Give the extent of all uninfected red blood cells.
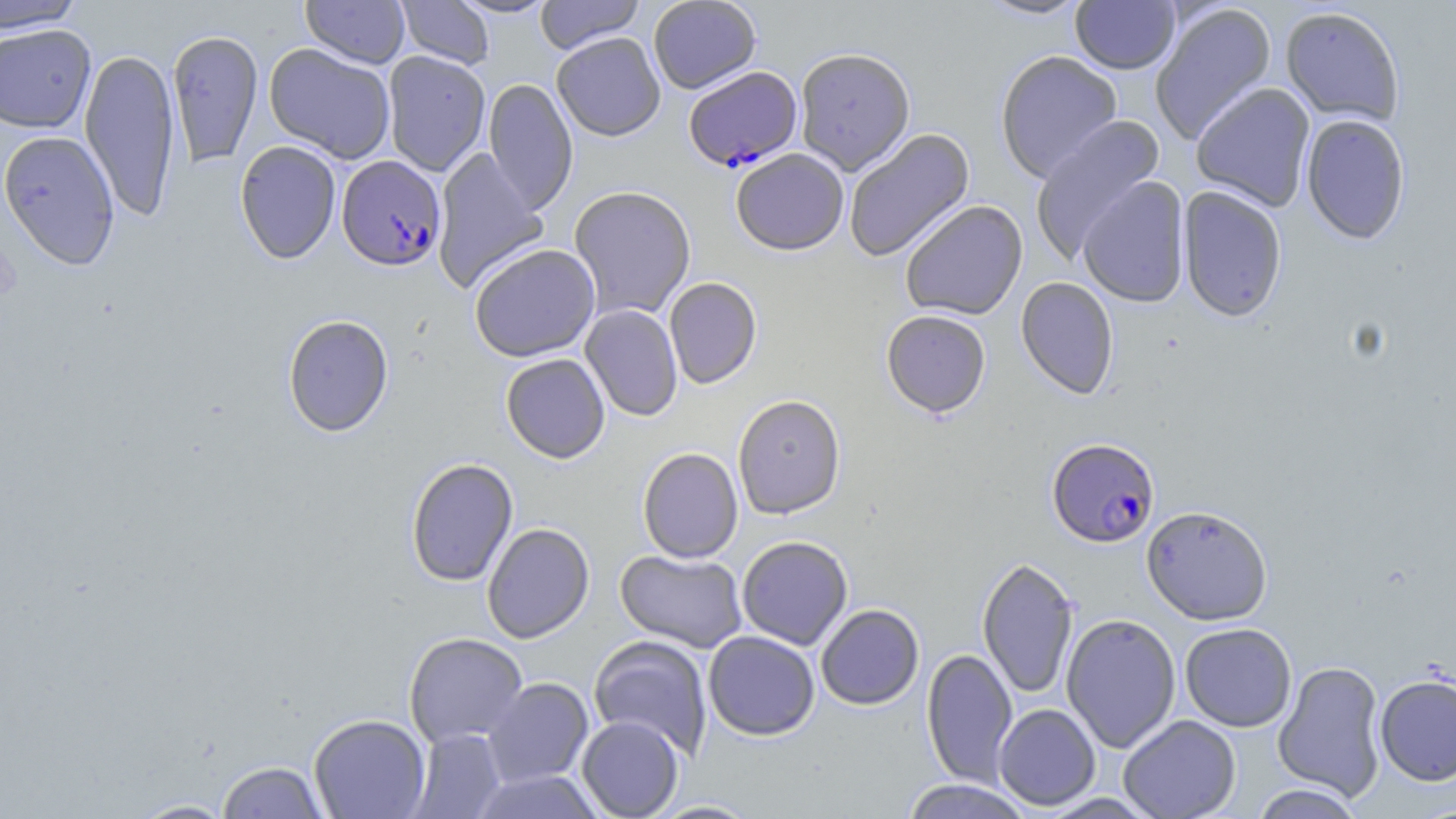

Approximate bounding boxes as named x1/y1/x2/y2 corners in pixels.
Uninfected red blood cells: (x1=0, y1=0, x2=85, y2=33), (x1=301, y1=0, x2=409, y2=68), (x1=395, y1=0, x2=494, y2=69), (x1=450, y1=0, x2=557, y2=18), (x1=535, y1=0, x2=645, y2=54), (x1=648, y1=0, x2=761, y2=94), (x1=976, y1=0, x2=1091, y2=21), (x1=1071, y1=1, x2=1180, y2=74), (x1=1149, y1=4, x2=1277, y2=145), (x1=1280, y1=6, x2=1405, y2=127), (x1=0, y1=24, x2=96, y2=133), (x1=166, y1=29, x2=264, y2=168), (x1=551, y1=32, x2=665, y2=141), (x1=264, y1=43, x2=396, y2=163), (x1=794, y1=46, x2=916, y2=175), (x1=79, y1=47, x2=181, y2=223), (x1=995, y1=50, x2=1123, y2=183), (x1=382, y1=51, x2=490, y2=176), (x1=483, y1=78, x2=579, y2=215), (x1=1191, y1=83, x2=1316, y2=212), (x1=1300, y1=114, x2=1411, y2=245), (x1=1029, y1=116, x2=1165, y2=262), (x1=844, y1=128, x2=975, y2=262), (x1=0, y1=130, x2=120, y2=270), (x1=234, y1=140, x2=342, y2=264), (x1=432, y1=147, x2=549, y2=294), (x1=730, y1=148, x2=849, y2=255), (x1=1078, y1=176, x2=1191, y2=308), (x1=568, y1=184, x2=696, y2=319), (x1=1178, y1=186, x2=1287, y2=322), (x1=899, y1=200, x2=1028, y2=321), (x1=469, y1=243, x2=600, y2=362), (x1=664, y1=277, x2=762, y2=389), (x1=1015, y1=277, x2=1119, y2=399), (x1=580, y1=304, x2=682, y2=422), (x1=881, y1=310, x2=991, y2=418), (x1=282, y1=313, x2=394, y2=437), (x1=500, y1=353, x2=610, y2=463), (x1=732, y1=394, x2=846, y2=519), (x1=637, y1=447, x2=743, y2=563), (x1=405, y1=458, x2=519, y2=587), (x1=1141, y1=505, x2=1273, y2=625), (x1=481, y1=522, x2=594, y2=643), (x1=736, y1=536, x2=853, y2=650), (x1=615, y1=548, x2=748, y2=652), (x1=976, y1=556, x2=1080, y2=700), (x1=815, y1=604, x2=924, y2=710), (x1=1061, y1=613, x2=1181, y2=753), (x1=1180, y1=623, x2=1297, y2=732), (x1=703, y1=631, x2=820, y2=741), (x1=404, y1=632, x2=528, y2=747), (x1=589, y1=635, x2=713, y2=759), (x1=921, y1=648, x2=1018, y2=787), (x1=1273, y1=661, x2=1388, y2=803), (x1=1374, y1=674, x2=1456, y2=786), (x1=483, y1=677, x2=594, y2=787), (x1=993, y1=703, x2=1101, y2=810), (x1=308, y1=713, x2=431, y2=818), (x1=1118, y1=714, x2=1241, y2=819), (x1=576, y1=715, x2=684, y2=819), (x1=408, y1=729, x2=507, y2=818), (x1=216, y1=761, x2=329, y2=819), (x1=469, y1=769, x2=605, y2=818), (x1=899, y1=778, x2=1035, y2=819), (x1=1250, y1=783, x2=1365, y2=818), (x1=1037, y1=793, x2=1163, y2=818), (x1=126, y1=798, x2=238, y2=818), (x1=646, y1=799, x2=763, y2=818).

slide-level diagnosis = Plasmodium falciparum
modality = optical microscopy
magnification = 1000x
image size = 1456×819 pixels
Plasmodium falciparum-infected red blood cell locations = approximate bounding boxes as named x1/y1/x2/y2 corners in pixels: (x1=683, y1=66, x2=802, y2=170), (x1=337, y1=155, x2=447, y2=271), (x1=1047, y1=438, x2=1160, y2=548)
preparation = thin blood film
field of view = one of a larger specimen
stain = May-Grünwald-Giemsa